Name the blood parasite species.
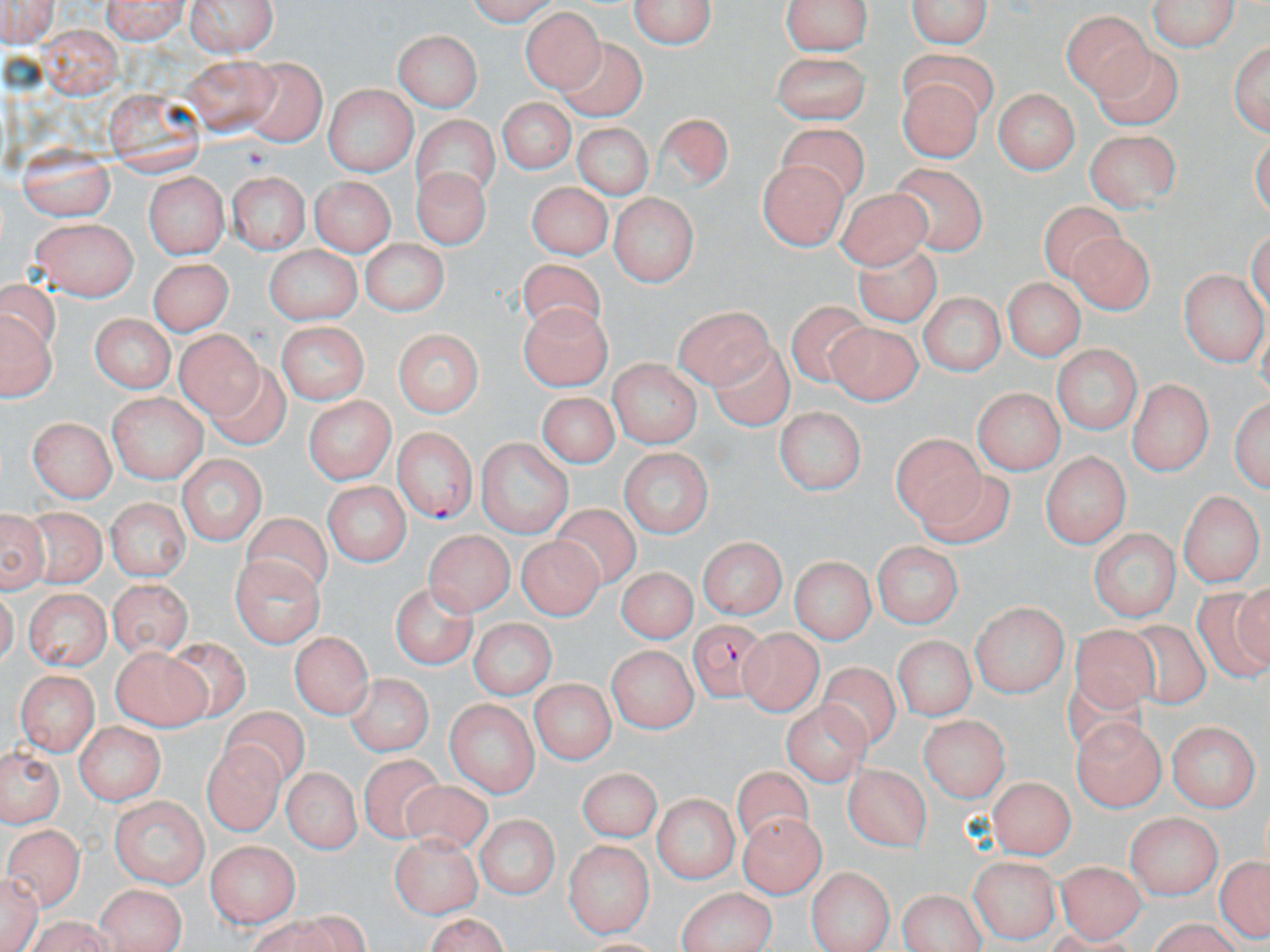
Plasmodium falciparum.

Approximate bounding boxes as named x1/y1/x2/y2 corners in pixels. Plasmodium falciparum-infected red blood cell locations: (x1=394, y1=425, x2=477, y2=523), (x1=688, y1=617, x2=776, y2=701). Uninfected red blood cell locations: (x1=0, y1=0, x2=60, y2=47), (x1=97, y1=0, x2=193, y2=40), (x1=188, y1=0, x2=276, y2=58), (x1=460, y1=0, x2=563, y2=21), (x1=629, y1=0, x2=720, y2=52), (x1=780, y1=0, x2=875, y2=57), (x1=906, y1=0, x2=994, y2=52), (x1=1146, y1=0, x2=1238, y2=51), (x1=1065, y1=5, x2=1154, y2=91), (x1=521, y1=8, x2=604, y2=94), (x1=40, y1=20, x2=122, y2=98), (x1=393, y1=29, x2=481, y2=111), (x1=1229, y1=34, x2=1268, y2=137), (x1=555, y1=39, x2=654, y2=123), (x1=769, y1=50, x2=872, y2=120), (x1=181, y1=54, x2=269, y2=134), (x1=244, y1=55, x2=328, y2=144), (x1=902, y1=77, x2=985, y2=159), (x1=321, y1=85, x2=418, y2=172), (x1=106, y1=87, x2=206, y2=177), (x1=990, y1=88, x2=1081, y2=174), (x1=498, y1=99, x2=571, y2=175), (x1=654, y1=112, x2=734, y2=192), (x1=408, y1=113, x2=501, y2=202), (x1=570, y1=121, x2=654, y2=199), (x1=771, y1=123, x2=869, y2=206), (x1=1086, y1=127, x2=1181, y2=207), (x1=13, y1=145, x2=113, y2=218), (x1=886, y1=159, x2=984, y2=256), (x1=758, y1=161, x2=845, y2=249), (x1=410, y1=166, x2=490, y2=247), (x1=144, y1=171, x2=231, y2=257), (x1=308, y1=174, x2=394, y2=253), (x1=230, y1=175, x2=309, y2=255), (x1=524, y1=178, x2=614, y2=253), (x1=836, y1=184, x2=930, y2=269), (x1=607, y1=194, x2=699, y2=286), (x1=1042, y1=198, x2=1132, y2=285), (x1=29, y1=218, x2=139, y2=302), (x1=1065, y1=228, x2=1152, y2=320), (x1=849, y1=235, x2=941, y2=327), (x1=359, y1=243, x2=447, y2=315), (x1=262, y1=244, x2=362, y2=326), (x1=150, y1=250, x2=230, y2=330), (x1=517, y1=258, x2=604, y2=344), (x1=1003, y1=271, x2=1086, y2=360), (x1=1181, y1=271, x2=1264, y2=364), (x1=916, y1=291, x2=1008, y2=375), (x1=786, y1=300, x2=870, y2=383), (x1=674, y1=301, x2=774, y2=384), (x1=518, y1=302, x2=609, y2=391), (x1=2, y1=310, x2=54, y2=400), (x1=86, y1=312, x2=178, y2=392), (x1=822, y1=320, x2=922, y2=405), (x1=275, y1=321, x2=369, y2=401), (x1=173, y1=323, x2=260, y2=416), (x1=392, y1=325, x2=484, y2=418), (x1=712, y1=333, x2=793, y2=435), (x1=1050, y1=344, x2=1139, y2=436), (x1=206, y1=358, x2=297, y2=448), (x1=606, y1=359, x2=703, y2=445), (x1=1130, y1=378, x2=1211, y2=476), (x1=971, y1=387, x2=1065, y2=472), (x1=108, y1=389, x2=210, y2=483), (x1=536, y1=389, x2=620, y2=466), (x1=1232, y1=392, x2=1268, y2=492), (x1=301, y1=393, x2=397, y2=484), (x1=775, y1=404, x2=864, y2=495), (x1=29, y1=414, x2=115, y2=502), (x1=890, y1=431, x2=991, y2=529), (x1=472, y1=438, x2=573, y2=536), (x1=620, y1=446, x2=711, y2=537), (x1=1040, y1=448, x2=1130, y2=550), (x1=174, y1=454, x2=266, y2=545), (x1=909, y1=467, x2=1008, y2=550), (x1=324, y1=480, x2=409, y2=569), (x1=1179, y1=488, x2=1263, y2=586), (x1=107, y1=495, x2=188, y2=579), (x1=23, y1=504, x2=110, y2=591), (x1=1, y1=506, x2=49, y2=595), (x1=550, y1=506, x2=639, y2=589), (x1=236, y1=513, x2=332, y2=603), (x1=1090, y1=525, x2=1180, y2=617), (x1=424, y1=528, x2=516, y2=612), (x1=700, y1=535, x2=785, y2=623), (x1=516, y1=537, x2=602, y2=619), (x1=872, y1=540, x2=961, y2=630), (x1=232, y1=553, x2=324, y2=648), (x1=790, y1=557, x2=873, y2=645), (x1=615, y1=565, x2=699, y2=643), (x1=389, y1=580, x2=474, y2=667), (x1=105, y1=581, x2=194, y2=651), (x1=1193, y1=585, x2=1270, y2=680), (x1=23, y1=587, x2=109, y2=670), (x1=969, y1=603, x2=1069, y2=696), (x1=1125, y1=617, x2=1209, y2=713), (x1=467, y1=618, x2=557, y2=698), (x1=1068, y1=624, x2=1165, y2=719), (x1=291, y1=628, x2=373, y2=717), (x1=739, y1=628, x2=822, y2=716), (x1=895, y1=636, x2=971, y2=718), (x1=162, y1=637, x2=249, y2=723), (x1=608, y1=642, x2=700, y2=732), (x1=109, y1=647, x2=209, y2=728), (x1=818, y1=659, x2=901, y2=750), (x1=1060, y1=666, x2=1148, y2=761), (x1=16, y1=667, x2=99, y2=754), (x1=345, y1=673, x2=431, y2=756), (x1=531, y1=676, x2=614, y2=764), (x1=782, y1=697, x2=873, y2=789), (x1=446, y1=699, x2=537, y2=798), (x1=219, y1=703, x2=313, y2=787), (x1=923, y1=716, x2=1008, y2=804), (x1=1074, y1=716, x2=1166, y2=809), (x1=1166, y1=720, x2=1258, y2=808), (x1=71, y1=725, x2=162, y2=803), (x1=202, y1=740, x2=286, y2=836), (x1=1, y1=746, x2=61, y2=829), (x1=356, y1=756, x2=446, y2=843), (x1=845, y1=764, x2=930, y2=849), (x1=279, y1=766, x2=363, y2=851), (x1=580, y1=768, x2=657, y2=841), (x1=732, y1=768, x2=819, y2=853), (x1=989, y1=777, x2=1073, y2=858), (x1=396, y1=780, x2=496, y2=863), (x1=654, y1=792, x2=739, y2=884), (x1=110, y1=797, x2=210, y2=886), (x1=735, y1=810, x2=825, y2=901), (x1=1126, y1=811, x2=1224, y2=900), (x1=474, y1=815, x2=559, y2=900), (x1=6, y1=821, x2=85, y2=908), (x1=388, y1=833, x2=483, y2=914), (x1=565, y1=838, x2=655, y2=936), (x1=206, y1=839, x2=303, y2=929), (x1=1215, y1=851, x2=1268, y2=944), (x1=1058, y1=857, x2=1143, y2=940), (x1=970, y1=858, x2=1059, y2=942), (x1=805, y1=862, x2=894, y2=952), (x1=1, y1=869, x2=41, y2=952), (x1=95, y1=880, x2=185, y2=952), (x1=678, y1=886, x2=778, y2=952), (x1=894, y1=889, x2=986, y2=950), (x1=245, y1=913, x2=370, y2=952), (x1=421, y1=913, x2=513, y2=952), (x1=19, y1=916, x2=122, y2=952). May-Grünwald-Giemsa-stained preparation. 1000x magnification. Thin blood smear. Optical microscopy. Single field of view. Image is 1270×952 pixels.